Locate and identify every blood parasite.
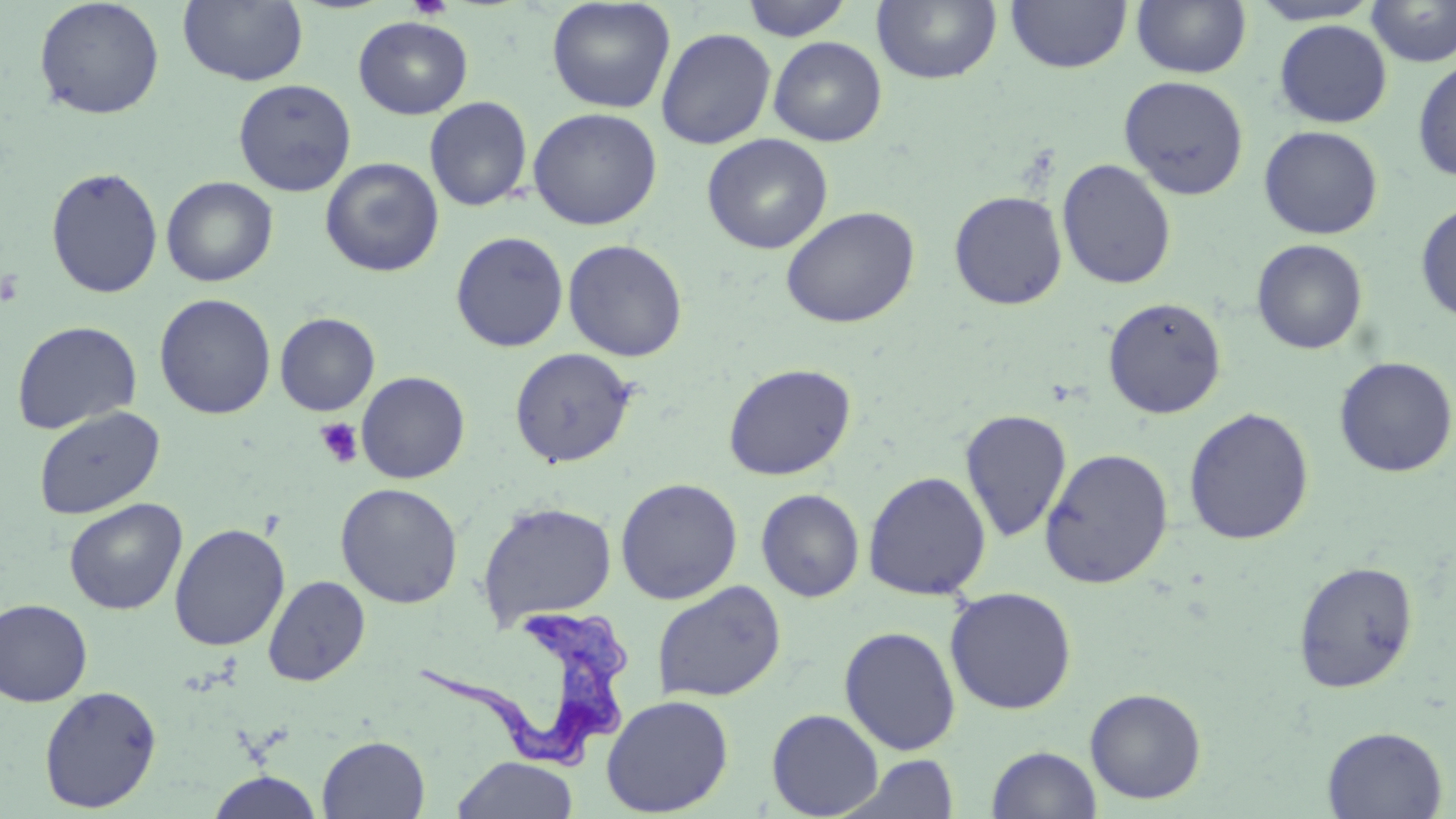

Approximate bounding boxes as (x1, y1, x2, y2) in pixels.
Trypanosoma brucei: (415, 608, 634, 770).
No Plasmodium falciparum, Plasmodium ovale, Plasmodium malariae, Plasmodium vivax, or Babesia divergens observed.

Summary:
  - Platelet locations: (407, 0, 453, 20), (315, 419, 363, 469)
  - Uninfected red blood cell locations: (33, 0, 165, 120), (178, 0, 308, 86), (546, 0, 676, 114), (740, 0, 854, 41), (1005, 0, 1132, 74), (1131, 0, 1252, 79), (1247, 0, 1384, 26), (1365, 0, 1456, 67), (872, 1, 1002, 85), (353, 16, 473, 119), (1274, 19, 1392, 128), (656, 27, 776, 149), (768, 36, 887, 146), (1412, 58, 1456, 183), (1119, 75, 1249, 200), (233, 79, 357, 196), (424, 96, 533, 212), (528, 107, 662, 230), (1259, 125, 1383, 240), (701, 133, 833, 254), (320, 157, 444, 277), (1056, 158, 1176, 290), (45, 166, 163, 298), (161, 176, 278, 287), (948, 190, 1068, 310), (1415, 200, 1456, 324), (780, 205, 920, 328), (450, 231, 569, 352), (1251, 238, 1368, 355), (563, 239, 688, 362), (154, 293, 276, 420), (1102, 297, 1227, 419), (275, 312, 380, 416), (11, 320, 142, 435), (509, 347, 637, 468), (1333, 356, 1455, 478), (722, 363, 856, 481), (356, 371, 470, 484), (33, 406, 165, 520), (1183, 407, 1314, 545), (959, 409, 1073, 542), (1039, 448, 1174, 588), (863, 470, 992, 601), (615, 477, 743, 605), (335, 482, 463, 609), (756, 488, 865, 602), (64, 498, 187, 615), (476, 500, 618, 629), (169, 523, 290, 652), (1293, 560, 1419, 694), (263, 575, 370, 687), (652, 580, 786, 704), (944, 586, 1077, 714), (0, 598, 93, 706), (839, 626, 961, 755), (38, 685, 162, 812), (1085, 687, 1207, 804), (600, 694, 734, 817), (766, 708, 884, 818), (1322, 725, 1448, 819), (317, 735, 429, 818), (987, 745, 1102, 819), (843, 755, 963, 819), (453, 756, 578, 818), (206, 770, 324, 818)
  - Slide-level diagnosis: Trypanosoma brucei
  - Preparation: thin blood film
  - Magnification: 1000x
  - Field of view: one of a larger specimen
  - Image size: 1456×819 pixels
  - Stain: May-Grünwald-Giemsa
  - Modality: optical microscopy